Report the malaria status of this cell.
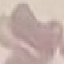

Uninfected.

Giemsa-stained preparation. Photographed with a smartphone camera at the microscope eyepiece. Thin blood film. Automatically extracted cell patch, resized to 64 × 64 pixels.